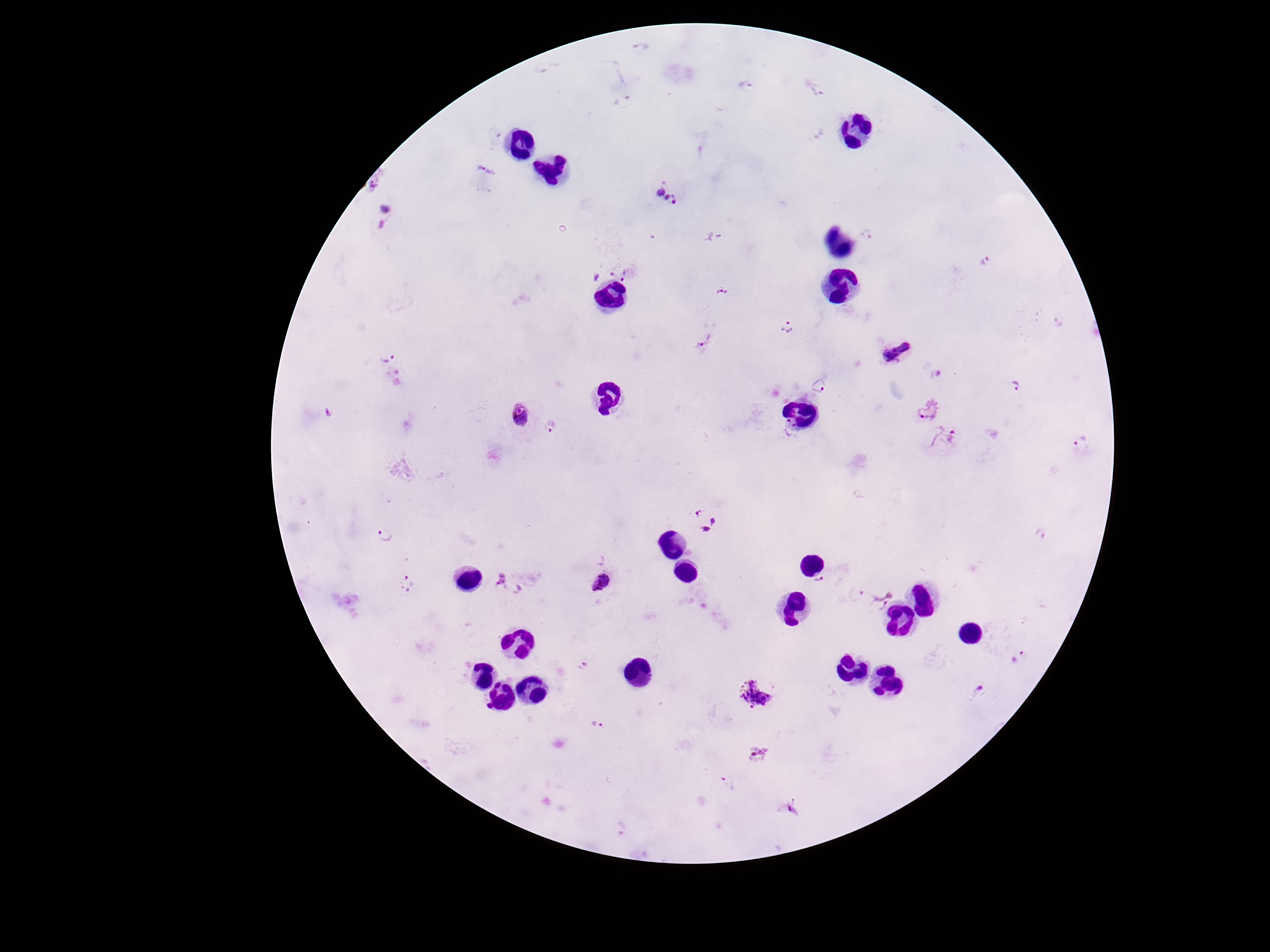

magnification = 100x
image size = 1270×952 pixels
patient malaria status = infected
preparation = thick blood film
field of view = one from this slide
capture = smartphone camera through the microscope eyepiece
Plasmodium parasite locations = approximate centers as {x, y} in pixels: {643, 48}, {745, 84}, {818, 90}, {622, 103}, {486, 172}, {374, 189}, {666, 197}, {386, 217}, {867, 235}, {712, 236}, {984, 261}, {624, 266}, {598, 274}, {722, 290}, {1059, 321}, {785, 327}, {704, 343}, {895, 350}, {387, 357}, {931, 371}, {1016, 386}, {820, 387}, {927, 409}, {328, 411}, {519, 416}, {551, 426}, {787, 428}, {945, 439}, {1081, 443}, {705, 520}, {1039, 535}, {384, 538}, {408, 581}, {820, 581}, {510, 583}, {599, 584}, {856, 594}, {880, 599}, {1020, 657}, {585, 666}, {978, 690}, {754, 693}, {598, 722}, {759, 755}, {728, 782}, {787, 810}
stain = Giemsa